Comment on the morphology of the red blood cells.
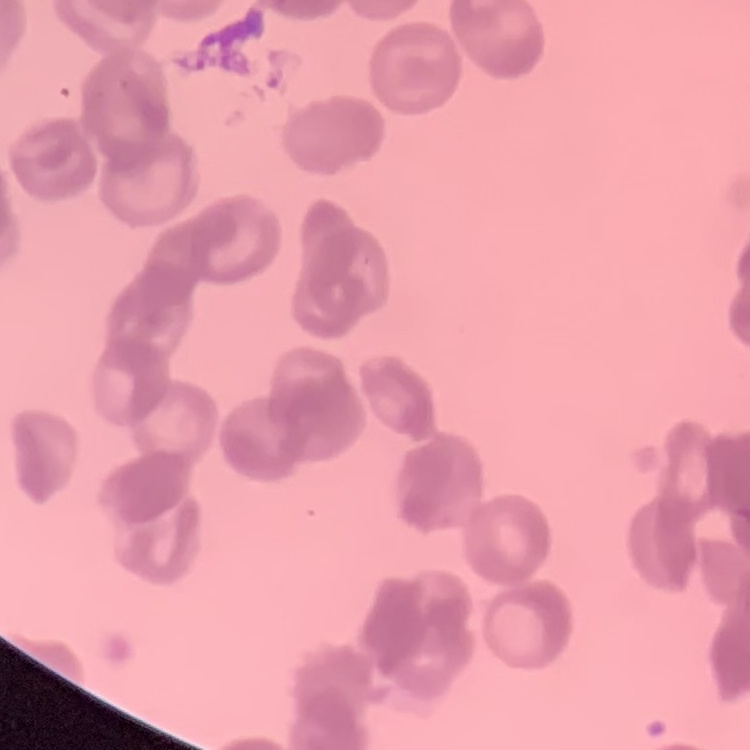
They show rouleaux formation.

Thin blood film. Square crop of a larger photomicrograph. Field's or Giemsa stain.